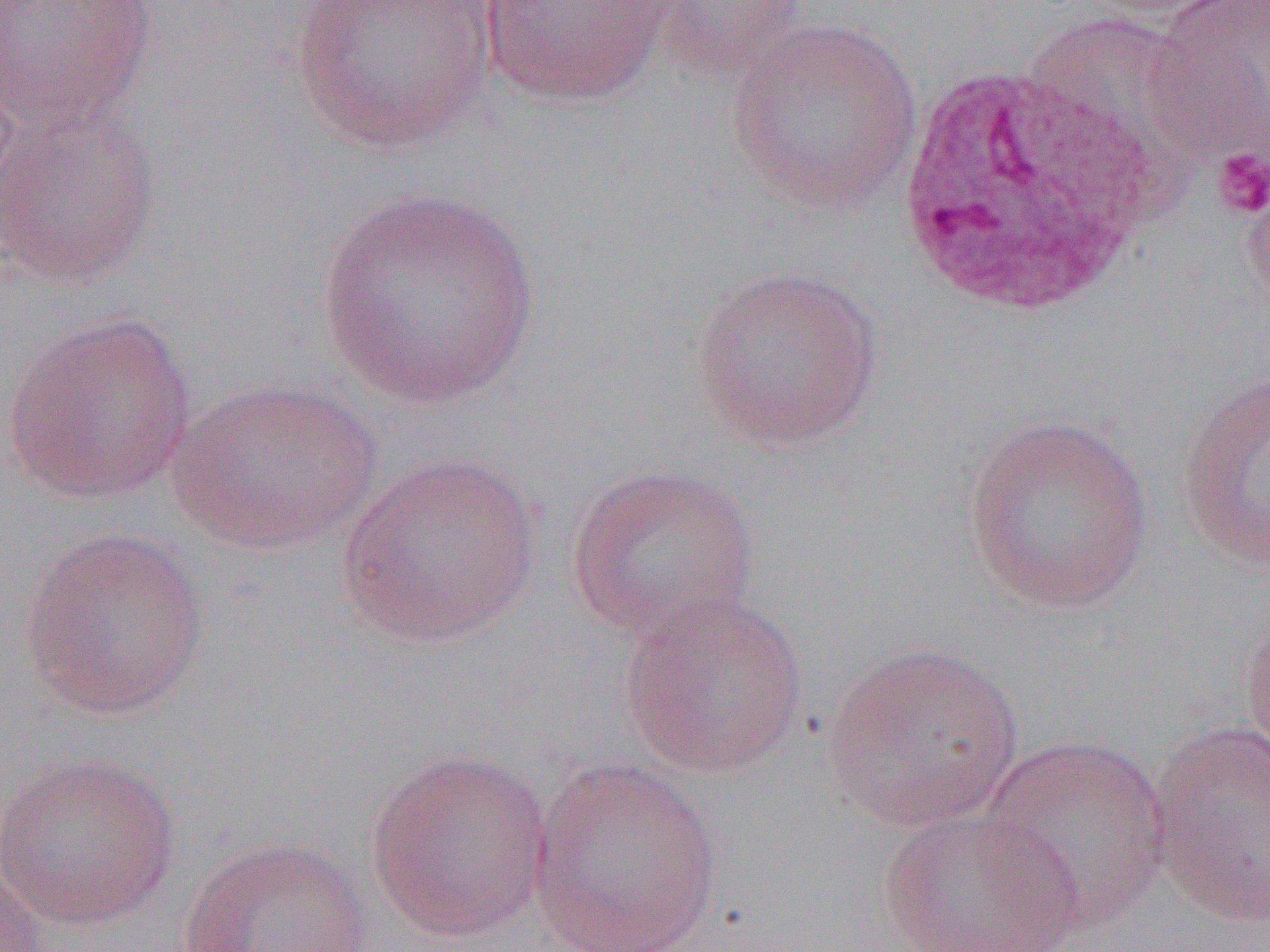

slide-level diagnosis = Plasmodium ovale
image size = 1270×952 pixels
modality = light microscopy
preparation = thin blood smear
field of view = one of a larger specimen
uninfected red blood cell locations = approximate bounding boxes as named x1/y1/x2/y2 corners in pixels: (x1=0, y1=0, x2=158, y2=132), (x1=1080, y1=0, x2=1242, y2=20), (x1=290, y1=1, x2=500, y2=153), (x1=475, y1=1, x2=678, y2=108), (x1=651, y1=1, x2=811, y2=84), (x1=1142, y1=4, x2=1270, y2=169), (x1=1019, y1=12, x2=1216, y2=206), (x1=725, y1=17, x2=925, y2=216), (x1=0, y1=61, x2=22, y2=222), (x1=0, y1=101, x2=162, y2=289), (x1=1240, y1=169, x2=1270, y2=323), (x1=317, y1=187, x2=543, y2=410), (x1=690, y1=265, x2=885, y2=452), (x1=2, y1=309, x2=198, y2=506), (x1=1175, y1=371, x2=1270, y2=573), (x1=165, y1=377, x2=384, y2=556), (x1=961, y1=414, x2=1155, y2=613), (x1=336, y1=451, x2=542, y2=648), (x1=566, y1=464, x2=759, y2=642), (x1=18, y1=526, x2=210, y2=721), (x1=617, y1=593, x2=810, y2=780), (x1=1239, y1=600, x2=1270, y2=768), (x1=823, y1=642, x2=1025, y2=833), (x1=1147, y1=721, x2=1269, y2=927), (x1=978, y1=734, x2=1172, y2=934), (x1=364, y1=749, x2=554, y2=944), (x1=1, y1=750, x2=180, y2=933), (x1=527, y1=757, x2=724, y2=952), (x1=877, y1=807, x2=1085, y2=951), (x1=175, y1=836, x2=374, y2=951), (x1=0, y1=865, x2=51, y2=952)
platelet locations = approximate bounding boxes as named x1/y1/x2/y2 corners in pixels: (x1=1211, y1=147, x2=1270, y2=219)
white blood cell locations = approximate bounding boxes as named x1/y1/x2/y2 corners in pixels: (x1=888, y1=59, x2=1164, y2=323)
magnification = 1000x